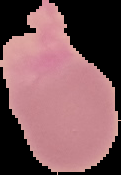
Segmented cell region on a black background. Malaria status: uninfected. Image is 121×175 pixels. From a thin blood smear.